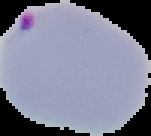

preparation = thin blood smear
image size = 151×136 pixels
image type = segmented cell region on a black background
malaria status = parasitized